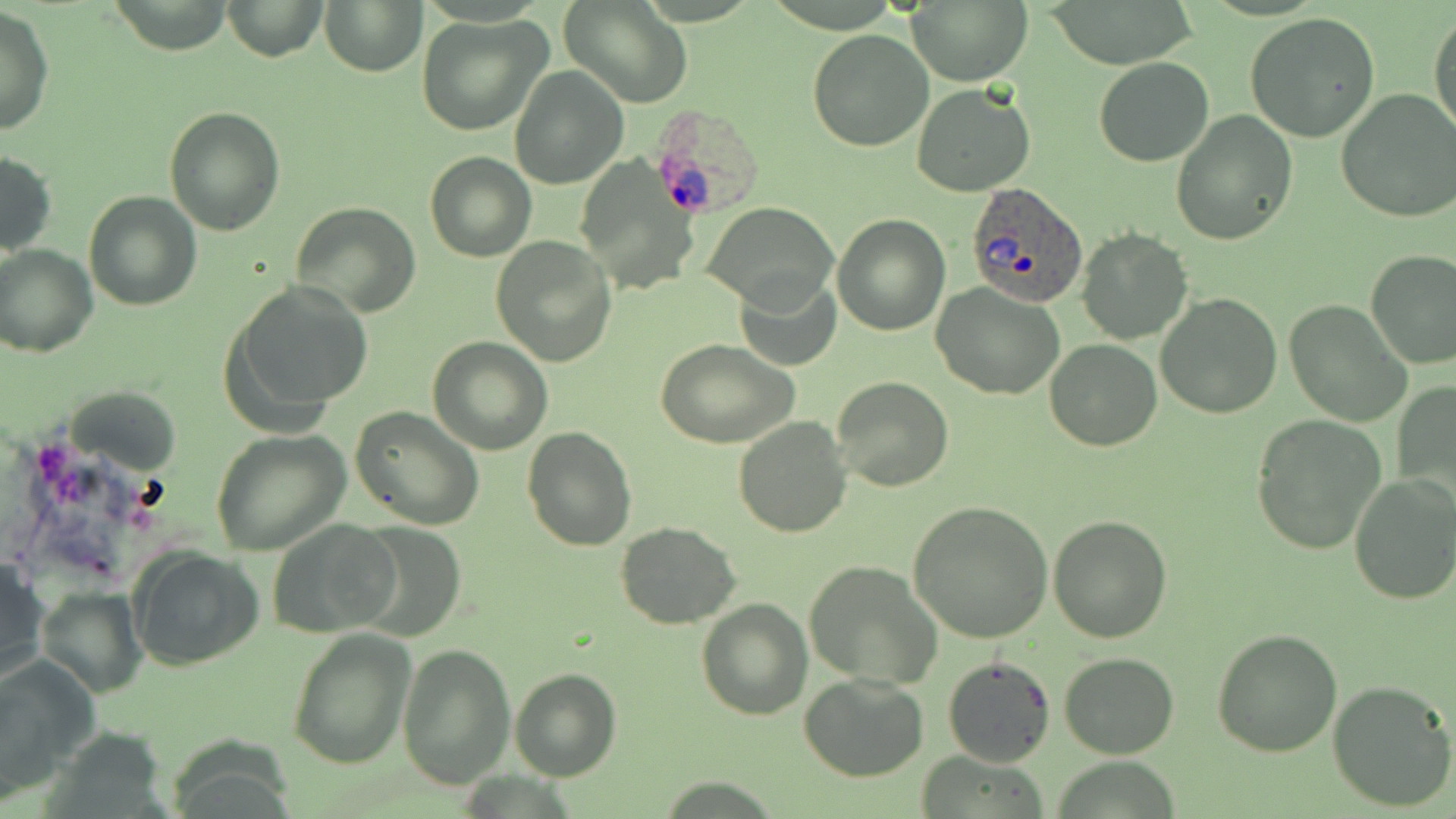

slide-level diagnosis = Plasmodium ovale
uninfected red blood cell locations = approximate bounding boxes as named x1/y1/x2/y2 corners in pixels: (x1=224, y1=0, x2=327, y2=61), (x1=561, y1=0, x2=693, y2=109), (x1=907, y1=0, x2=1032, y2=86), (x1=1041, y1=0, x2=1200, y2=66), (x1=106, y1=1, x2=234, y2=53), (x1=322, y1=1, x2=425, y2=75), (x1=0, y1=7, x2=53, y2=136), (x1=1429, y1=11, x2=1455, y2=140), (x1=1245, y1=12, x2=1381, y2=143), (x1=415, y1=15, x2=551, y2=136), (x1=807, y1=30, x2=933, y2=152), (x1=1094, y1=56, x2=1214, y2=166), (x1=510, y1=66, x2=628, y2=189), (x1=912, y1=85, x2=1036, y2=197), (x1=1336, y1=90, x2=1456, y2=224), (x1=164, y1=105, x2=285, y2=234), (x1=1170, y1=110, x2=1296, y2=246), (x1=425, y1=151, x2=535, y2=262), (x1=0, y1=152, x2=57, y2=256), (x1=83, y1=190, x2=201, y2=311), (x1=704, y1=201, x2=836, y2=307), (x1=291, y1=202, x2=421, y2=317), (x1=832, y1=214, x2=951, y2=335), (x1=1077, y1=229, x2=1191, y2=344), (x1=492, y1=238, x2=617, y2=367), (x1=0, y1=245, x2=97, y2=358), (x1=1365, y1=249, x2=1456, y2=370), (x1=733, y1=274, x2=841, y2=371), (x1=227, y1=280, x2=374, y2=423), (x1=931, y1=285, x2=1064, y2=400), (x1=1156, y1=292, x2=1282, y2=419), (x1=1284, y1=299, x2=1412, y2=428), (x1=429, y1=337, x2=551, y2=455), (x1=656, y1=339, x2=799, y2=449), (x1=1044, y1=340, x2=1162, y2=451), (x1=831, y1=376, x2=955, y2=492), (x1=1393, y1=379, x2=1456, y2=507), (x1=67, y1=386, x2=180, y2=471), (x1=349, y1=407, x2=485, y2=532), (x1=1249, y1=414, x2=1387, y2=555), (x1=732, y1=416, x2=851, y2=537), (x1=521, y1=426, x2=636, y2=550), (x1=211, y1=430, x2=349, y2=555), (x1=1348, y1=474, x2=1456, y2=606), (x1=906, y1=501, x2=1052, y2=642), (x1=1048, y1=515, x2=1175, y2=643), (x1=270, y1=519, x2=401, y2=636), (x1=351, y1=521, x2=464, y2=638), (x1=615, y1=522, x2=740, y2=628), (x1=129, y1=546, x2=264, y2=671), (x1=0, y1=558, x2=50, y2=689), (x1=804, y1=561, x2=942, y2=688), (x1=38, y1=587, x2=148, y2=699), (x1=696, y1=598, x2=813, y2=720), (x1=286, y1=627, x2=416, y2=770), (x1=1212, y1=629, x2=1343, y2=756), (x1=399, y1=644, x2=513, y2=786), (x1=1058, y1=653, x2=1180, y2=759), (x1=0, y1=654, x2=98, y2=798), (x1=941, y1=654, x2=1055, y2=768), (x1=509, y1=669, x2=622, y2=781), (x1=799, y1=672, x2=929, y2=780), (x1=1327, y1=679, x2=1455, y2=812)
Plasmodium ovale-infected red blood cell locations = approximate bounding boxes as named x1/y1/x2/y2 corners in pixels: (x1=653, y1=103, x2=758, y2=221), (x1=964, y1=182, x2=1090, y2=306)
field of view = one of a larger specimen
image size = 1456×819 pixels
preparation = thin blood film
stain = May-Grünwald-Giemsa
magnification = 1000x
modality = optical microscopy